Classify this cell by malaria status.
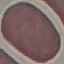

It is uninfected.

Summary:
  - Image type: cell patch, automatically extracted from a larger field of view and resized to 64 × 64 pixels
  - Capture: smartphone camera at the microscope eyepiece
  - Stain: Giemsa
  - Preparation: thin blood film